Describe the morphology of the red blood cells.
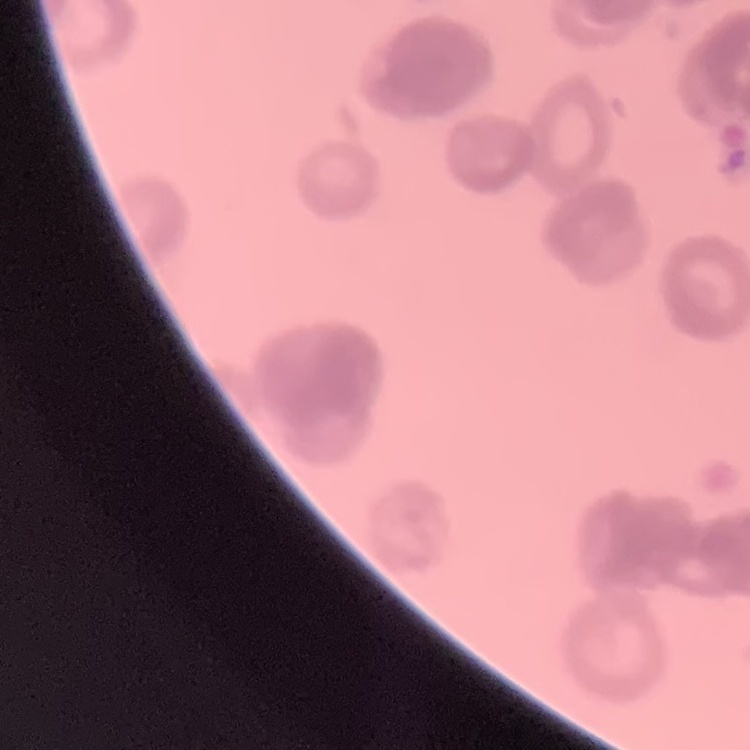

Rouleaux formation.

Summary:
  - Stain: Field's or Giemsa
  - Preparation: thin peripheral smear
  - Image type: square crop of a larger photomicrograph